Comment on the morphology of the erythrocytes.
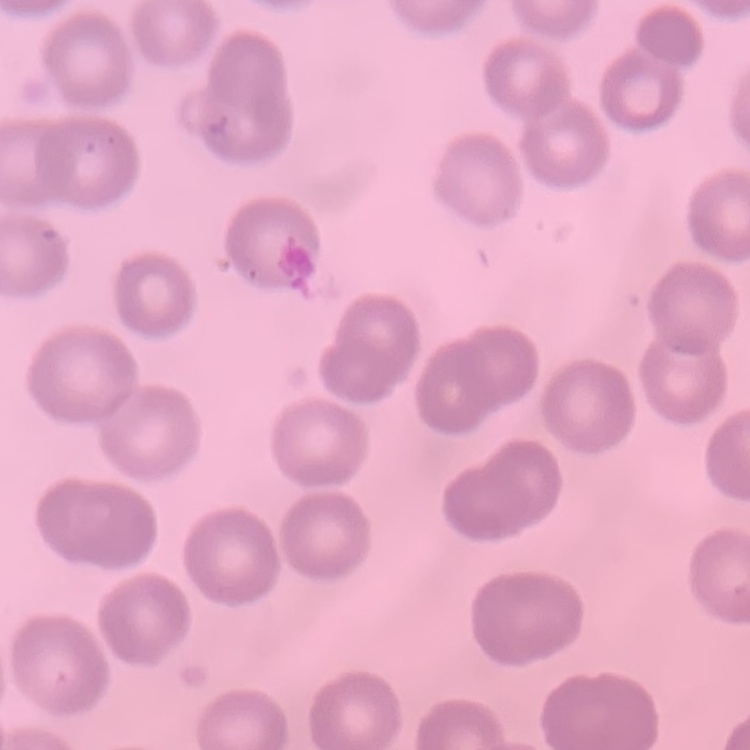

No rouleaux formation.

Summary:
  - Image type: one tile cut from a larger photomicrograph
  - Preparation: thin blood film
  - Stain: Field's or Giemsa